State which parasite is depicted.
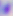
Toxoplasma gondii.

modality: photomicrograph
magnification: 400x